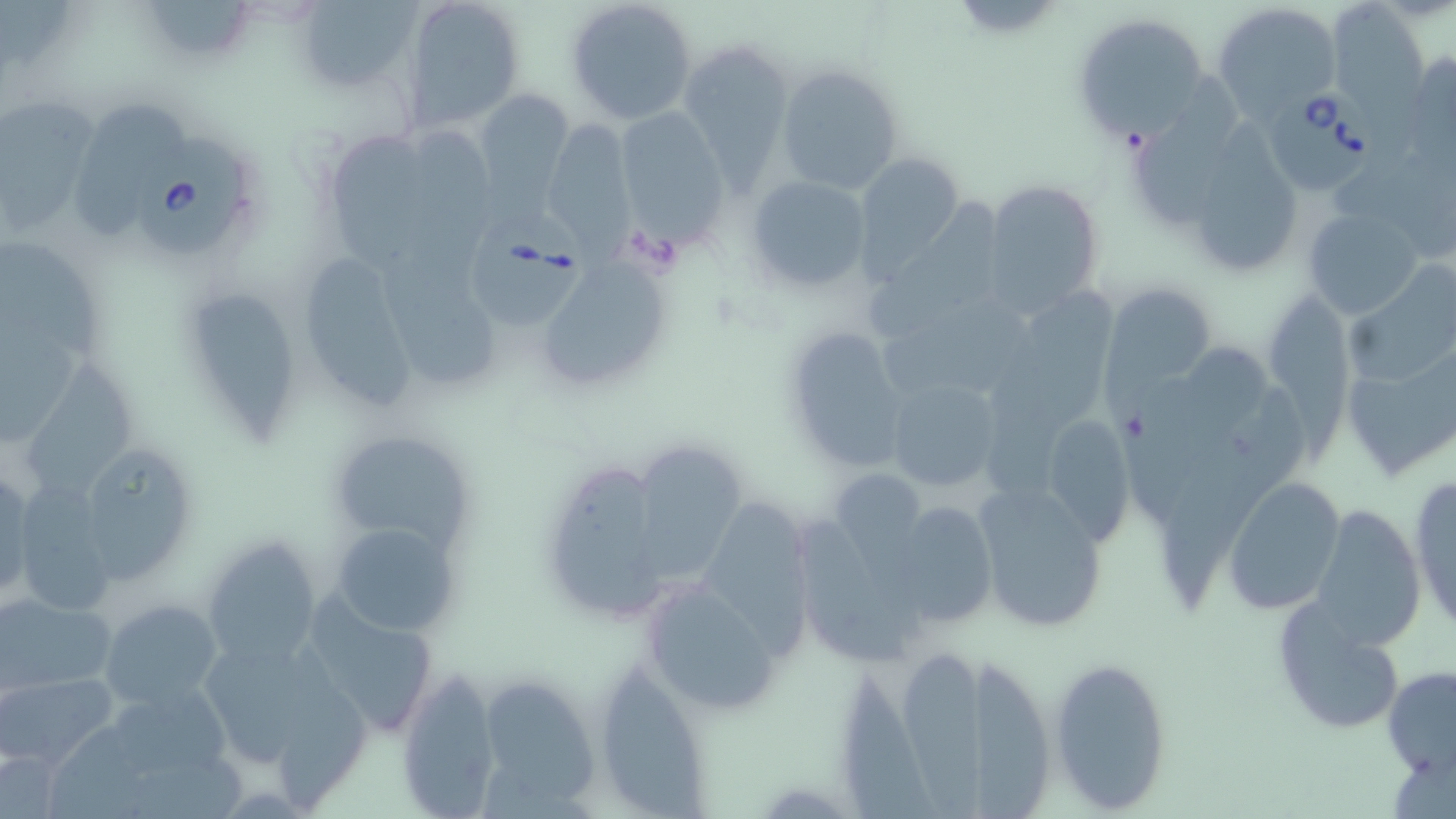

Summary:
  - Coordinate format: approximate bounding boxes as [x1, y1, x2, y2] in pixels
  - Babesia divergens-infected red blood cell locations: [1268, 86, 1380, 194], [138, 145, 251, 258], [469, 207, 587, 332]
  - Uninfected red blood cell locations: [2, 0, 74, 67], [148, 0, 253, 59], [401, 0, 526, 131], [566, 0, 698, 125], [1214, 1, 1345, 121], [296, 2, 419, 93], [1326, 3, 1429, 114], [1070, 13, 1213, 143], [679, 38, 795, 182], [1402, 50, 1456, 166], [775, 62, 906, 195], [1142, 77, 1237, 230], [472, 88, 576, 198], [0, 99, 98, 227], [73, 102, 191, 239], [614, 106, 729, 240], [541, 118, 637, 253], [1199, 118, 1302, 272], [405, 121, 496, 293], [332, 134, 430, 271], [851, 151, 965, 277], [1331, 155, 1456, 257], [746, 175, 873, 293], [980, 177, 1104, 314], [867, 198, 1000, 333], [1303, 207, 1426, 320], [382, 235, 499, 389], [0, 241, 106, 356], [536, 254, 672, 390], [304, 257, 412, 412], [1345, 272, 1455, 388], [1103, 286, 1215, 403], [990, 289, 1116, 491], [198, 294, 294, 445], [1269, 294, 1346, 471], [883, 295, 1030, 395], [0, 307, 81, 441], [782, 327, 912, 473], [1108, 343, 1263, 527], [1343, 351, 1453, 481], [23, 352, 139, 508], [884, 377, 1004, 494], [1161, 384, 1306, 607], [1038, 412, 1138, 549], [327, 427, 479, 556], [72, 439, 199, 585], [638, 445, 752, 581], [553, 464, 661, 617], [0, 467, 31, 601], [1222, 475, 1345, 612], [1407, 475, 1456, 633], [833, 477, 928, 640], [971, 479, 1108, 633], [7, 482, 117, 615], [697, 494, 805, 669], [887, 500, 996, 628], [1310, 502, 1426, 651], [795, 515, 912, 669], [329, 521, 460, 638], [200, 534, 326, 668], [636, 578, 784, 714], [305, 592, 442, 736], [0, 594, 118, 693], [101, 598, 224, 708], [1273, 598, 1407, 736], [193, 630, 372, 790], [1048, 653, 1174, 812], [905, 654, 989, 819], [592, 656, 712, 817], [972, 657, 1052, 818], [848, 661, 935, 819], [1382, 666, 1456, 777], [396, 667, 501, 818], [477, 670, 603, 810], [3, 671, 117, 770], [105, 686, 233, 773], [0, 742, 67, 819]
  - Slide-level diagnosis: Babesia divergens
  - Modality: optical microscopy
  - Field of view: single
  - Image size: 1456×819 pixels
  - Magnification: 1000x
  - Stain: May-Grünwald-Giemsa
  - Preparation: thin blood smear